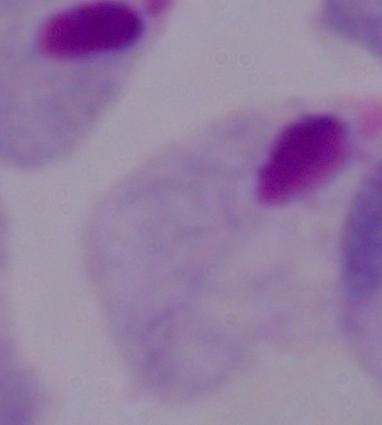
A trichomonad is seen. Micrograph. 1000x magnification.